Name the parasite shown.
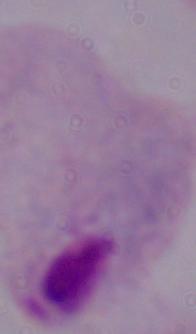
A trichomonad.

magnification = 1000x
modality = micrograph